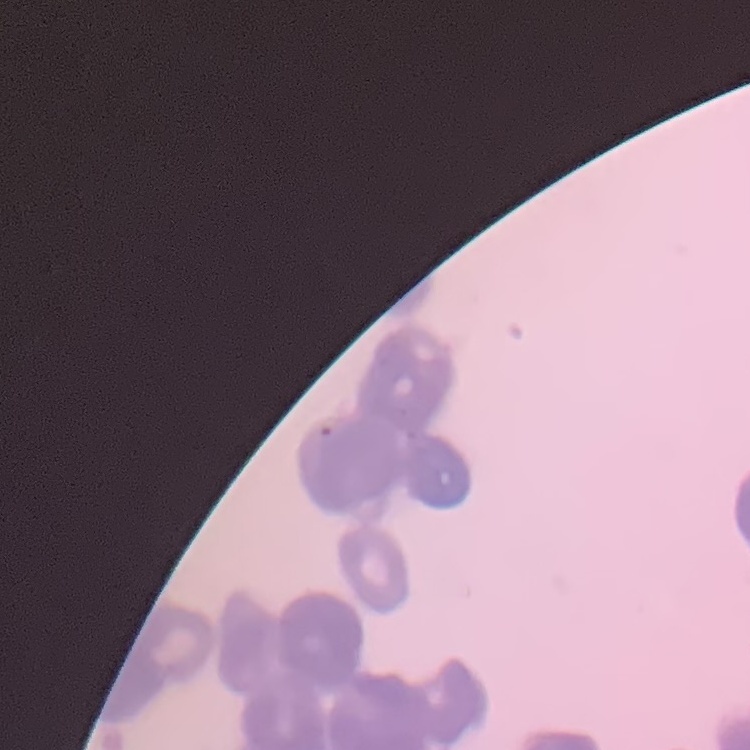
erythrocyte morphology = rouleaux formation
image type = one tile cut from a larger photomicrograph
preparation = thin blood film
stain = Field's or Giemsa